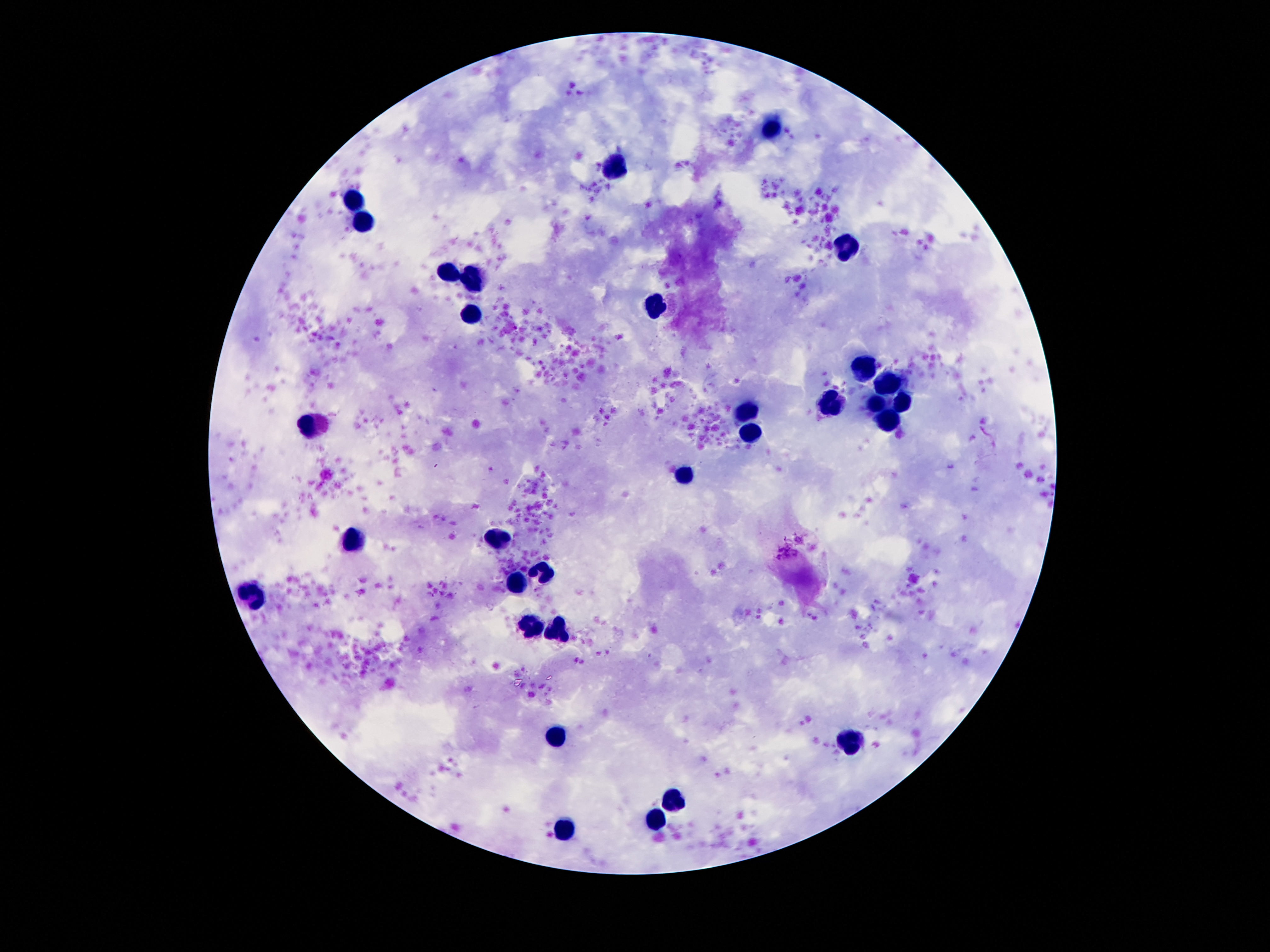

Approximate centers as [x, y] in pixels.
Summary:
  - Leukocyte locations: [771, 128], [614, 169], [351, 204], [363, 223], [845, 247], [450, 274], [472, 282], [659, 304], [470, 315], [860, 366], [890, 389], [905, 403], [878, 405], [831, 409], [745, 415], [888, 421], [312, 425], [751, 435], [687, 477], [497, 539], [349, 542], [548, 571], [517, 583], [255, 598], [530, 626], [558, 631], [554, 735], [853, 738], [675, 799], [655, 819], [564, 831]
  - Capture: smartphone camera through the microscope eyepiece
  - Stain: Giemsa
  - Patient malaria status: uninfected
  - Magnification: 100x
  - Field of view: one from this slide
  - Preparation: thick blood smear
  - Image size: 1270×952 pixels